Assess for Plasmodium parasites.
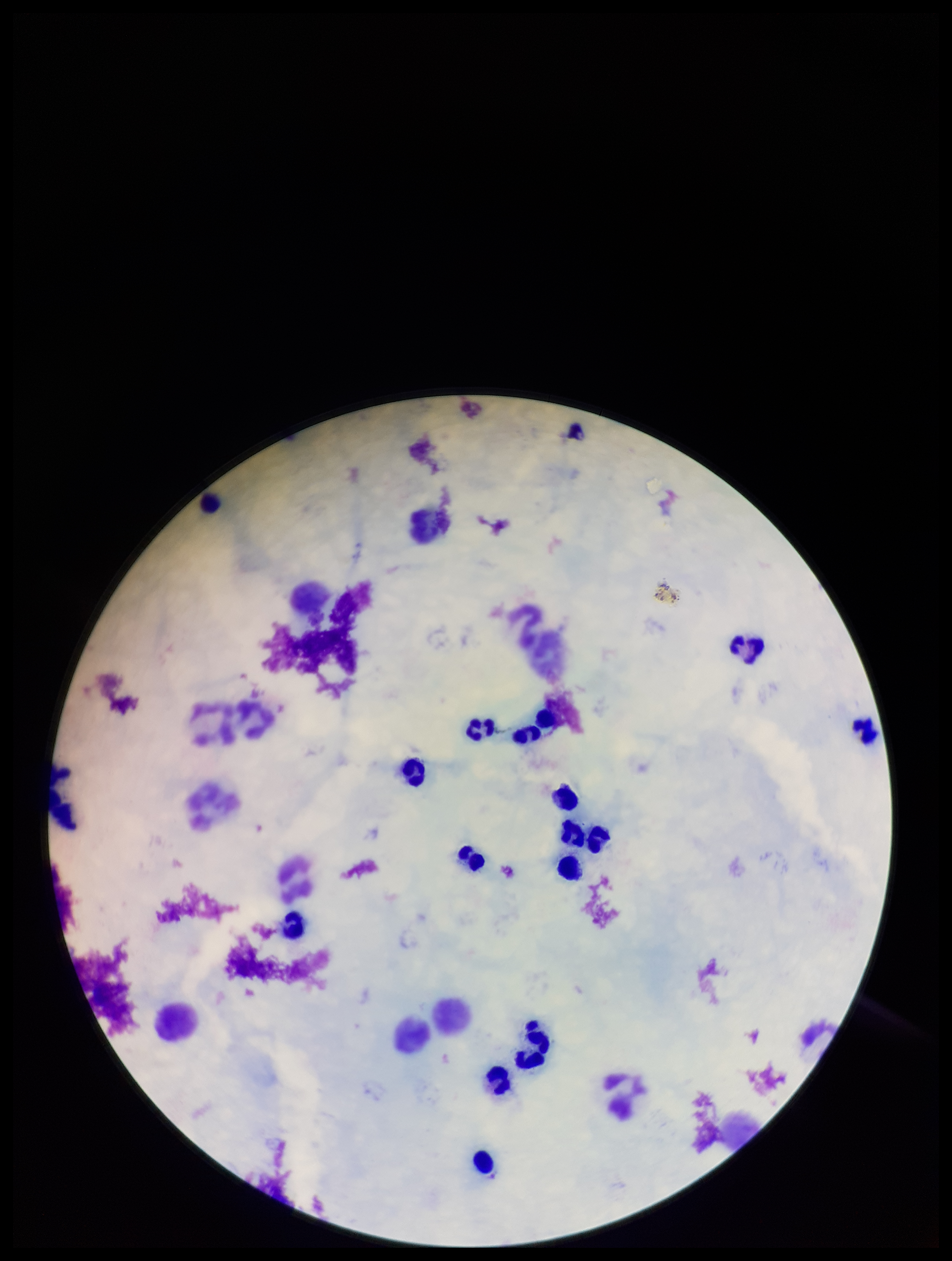

None identified.

Summary:
  - Field of view: one from this slide
  - Capture: smartphone photograph through the microscope eyepiece
  - Image size: 952×1261 pixels
  - Patient malaria status: negative
  - Leukocyte count: 16
  - Stain: Giemsa
  - Preparation: thick
  - Parasite count: 0